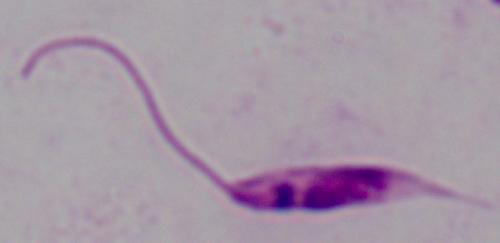

A Leishmania parasite is seen. Micrograph. 1000x magnification.